Name the blood parasite species.
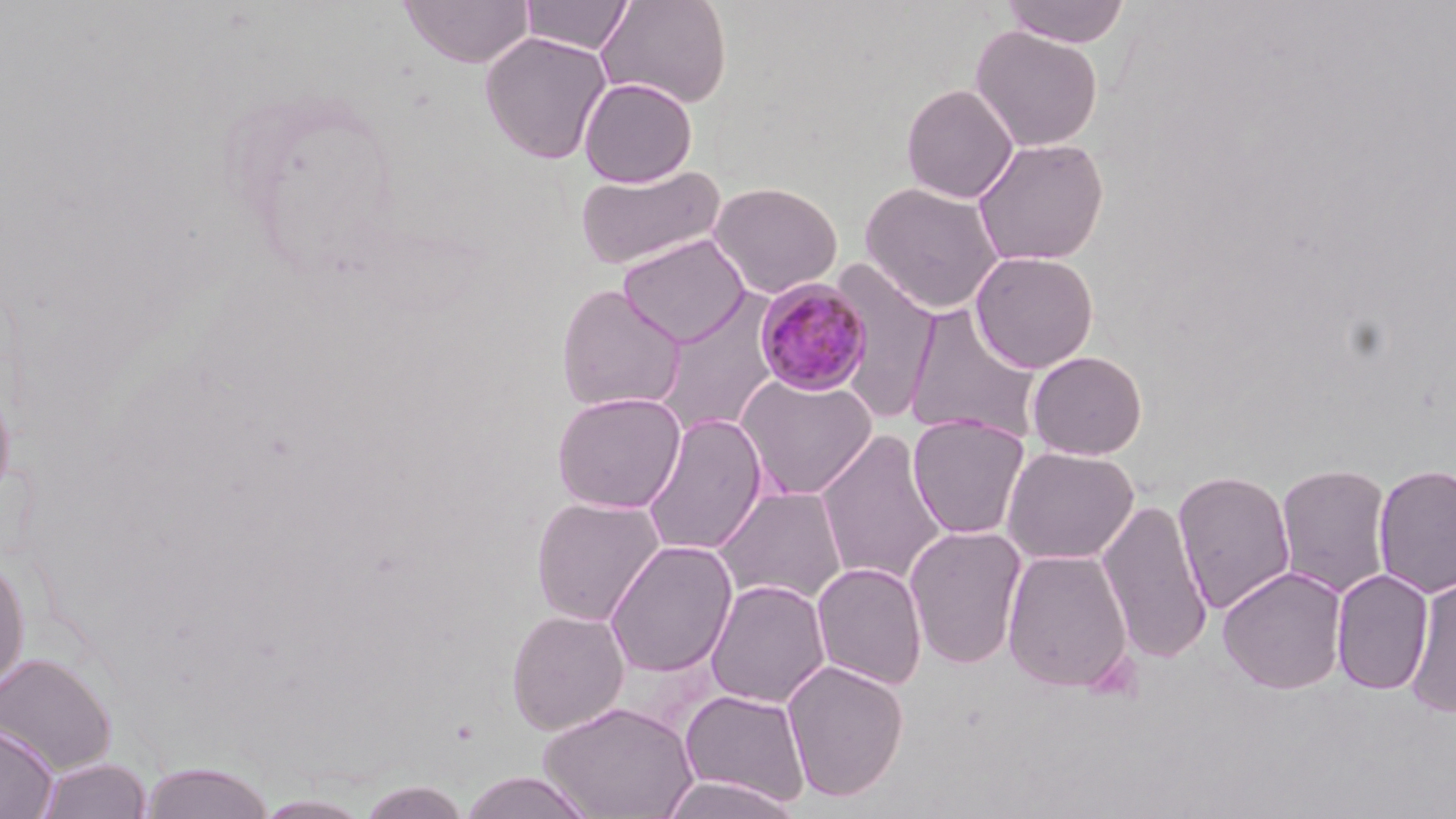

Plasmodium malariae.

image size = 1456×819 pixels
uninfected red blood cell locations = approximate bounding boxes as [x1, y1, x2, y2] in pixels: [399, 0, 534, 68], [520, 0, 633, 55], [596, 0, 732, 108], [1000, 0, 1131, 48], [970, 25, 1103, 152], [479, 31, 613, 164], [578, 76, 698, 187], [901, 83, 1019, 203], [972, 136, 1109, 266], [573, 164, 727, 271], [709, 181, 843, 299], [860, 181, 1005, 314], [618, 233, 750, 348], [970, 250, 1099, 373], [829, 258, 940, 425], [555, 284, 687, 412], [652, 292, 783, 437], [904, 305, 1043, 443], [1027, 350, 1148, 460], [735, 372, 879, 501], [0, 378, 16, 508], [551, 390, 687, 513], [641, 412, 768, 556], [907, 414, 1030, 539], [814, 430, 948, 586], [1001, 445, 1140, 566], [1275, 462, 1393, 599], [1372, 463, 1456, 599], [1173, 469, 1296, 615], [713, 485, 848, 606], [530, 495, 665, 626], [1097, 496, 1213, 664], [904, 524, 1028, 669], [605, 540, 738, 677], [1002, 548, 1133, 694], [0, 551, 30, 697], [811, 561, 928, 690], [1217, 565, 1348, 694], [1331, 568, 1434, 695], [705, 578, 831, 709], [1404, 578, 1456, 717], [505, 608, 630, 735], [0, 652, 117, 774], [782, 659, 910, 802], [679, 688, 812, 809], [537, 700, 699, 819], [0, 720, 58, 819], [35, 757, 152, 819], [138, 762, 277, 819], [458, 771, 597, 818], [656, 775, 805, 819], [356, 781, 472, 819], [253, 793, 376, 818]
modality = optical microscopy
magnification = 1000x
preparation = thin blood smear
Plasmodium malariae-infected red blood cell locations = approximate bounding boxes as [x1, y1, x2, y2] in pixels: [753, 277, 873, 396]
stain = May-Grünwald-Giemsa
field of view = single